Give the position of every malaria parasite.
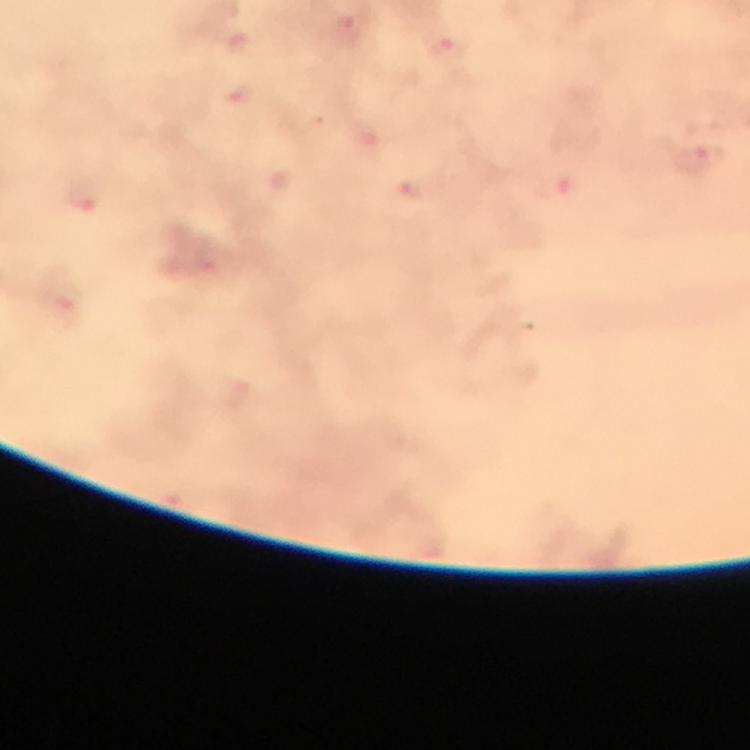
Approximate centers as {x, y} in pixels.
Malaria parasites: {693, 160}, {411, 189}.

immersion_oil: applied
cropped_from: one field of view
context: from a diagnostic examination for malaria
preparation: thick blood film
magnification: 100x
stain: Giemsa
capture: smartphone mounted on the microscope
image_size: 750×750 pixels